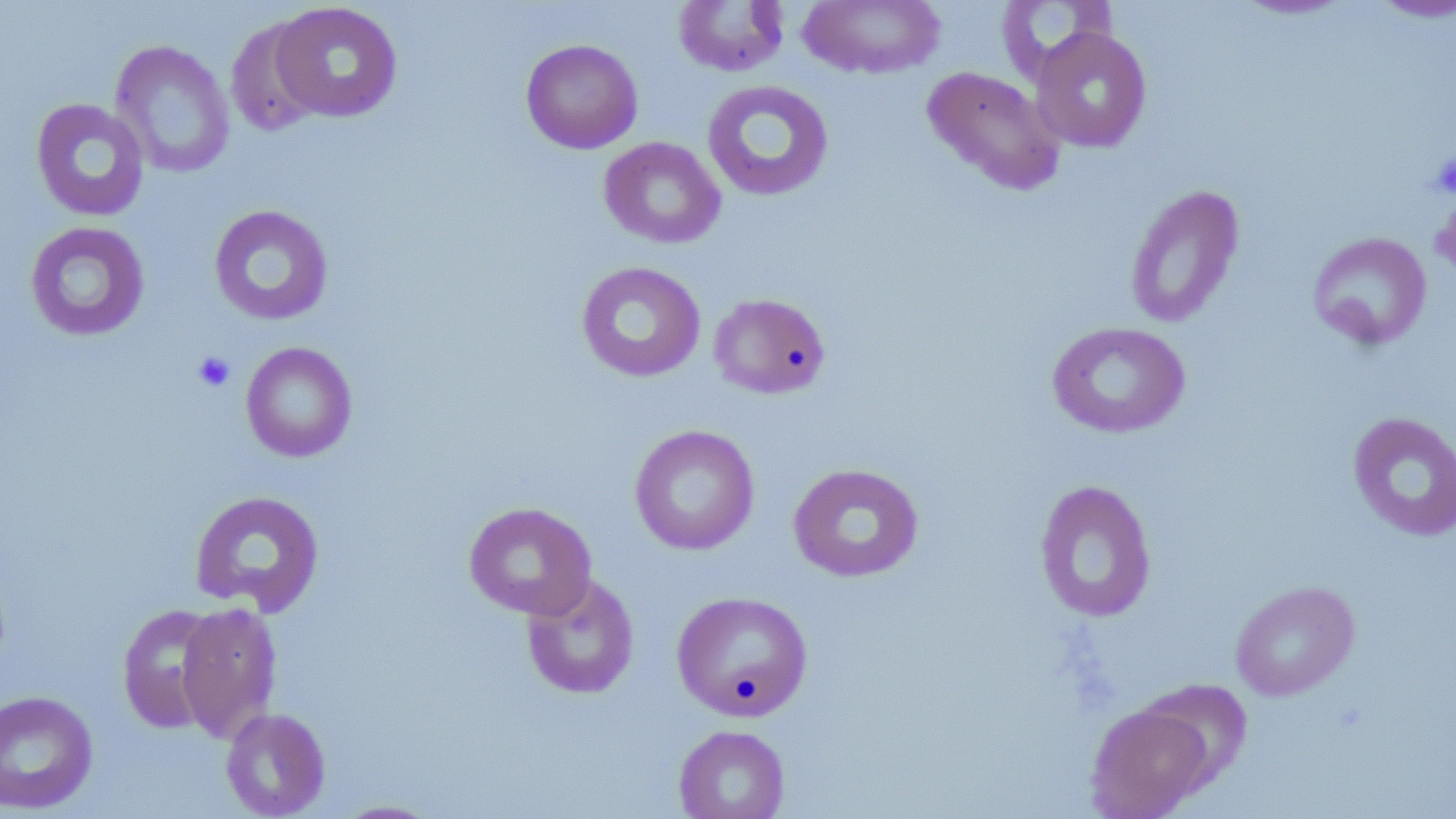

slide-level diagnosis = no evidence of blood parasites
image size = 1456×819 pixels
stain = May-Grünwald-Giemsa
platelet locations = approximate bounding boxes as named x1/y1/x2/y2 corners in pixels: (x1=1429, y1=153, x2=1456, y2=199), (x1=191, y1=350, x2=236, y2=393)
preparation = thin blood smear
modality = light microscopy
magnification = 1000x
uninfected red blood cell locations = approximate bounding boxes as named x1/y1/x2/y2 corners in pixels: (x1=798, y1=0, x2=945, y2=79), (x1=996, y1=0, x2=1118, y2=82), (x1=1228, y1=0, x2=1359, y2=21), (x1=1366, y1=0, x2=1456, y2=23), (x1=672, y1=1, x2=790, y2=77), (x1=269, y1=2, x2=404, y2=123), (x1=225, y1=16, x2=326, y2=137), (x1=1030, y1=27, x2=1153, y2=153), (x1=520, y1=38, x2=643, y2=154), (x1=111, y1=40, x2=235, y2=179), (x1=921, y1=66, x2=1066, y2=196), (x1=701, y1=79, x2=835, y2=202), (x1=30, y1=98, x2=150, y2=222), (x1=599, y1=136, x2=726, y2=249), (x1=1124, y1=184, x2=1245, y2=328), (x1=208, y1=204, x2=334, y2=326), (x1=24, y1=221, x2=151, y2=342), (x1=1307, y1=231, x2=1432, y2=350), (x1=576, y1=261, x2=707, y2=383), (x1=708, y1=292, x2=831, y2=400), (x1=1046, y1=321, x2=1191, y2=439), (x1=240, y1=342, x2=358, y2=462), (x1=1347, y1=411, x2=1456, y2=542), (x1=629, y1=424, x2=760, y2=555), (x1=787, y1=463, x2=924, y2=582), (x1=1033, y1=479, x2=1157, y2=622), (x1=189, y1=490, x2=325, y2=616), (x1=463, y1=502, x2=597, y2=620), (x1=521, y1=573, x2=640, y2=700), (x1=1229, y1=579, x2=1360, y2=701), (x1=671, y1=590, x2=813, y2=721), (x1=175, y1=601, x2=283, y2=742), (x1=116, y1=603, x2=223, y2=734), (x1=1137, y1=678, x2=1254, y2=790), (x1=0, y1=690, x2=100, y2=814), (x1=1085, y1=703, x2=1213, y2=818), (x1=220, y1=707, x2=330, y2=818), (x1=673, y1=724, x2=791, y2=819), (x1=332, y1=800, x2=443, y2=818)
field of view = one of a larger specimen